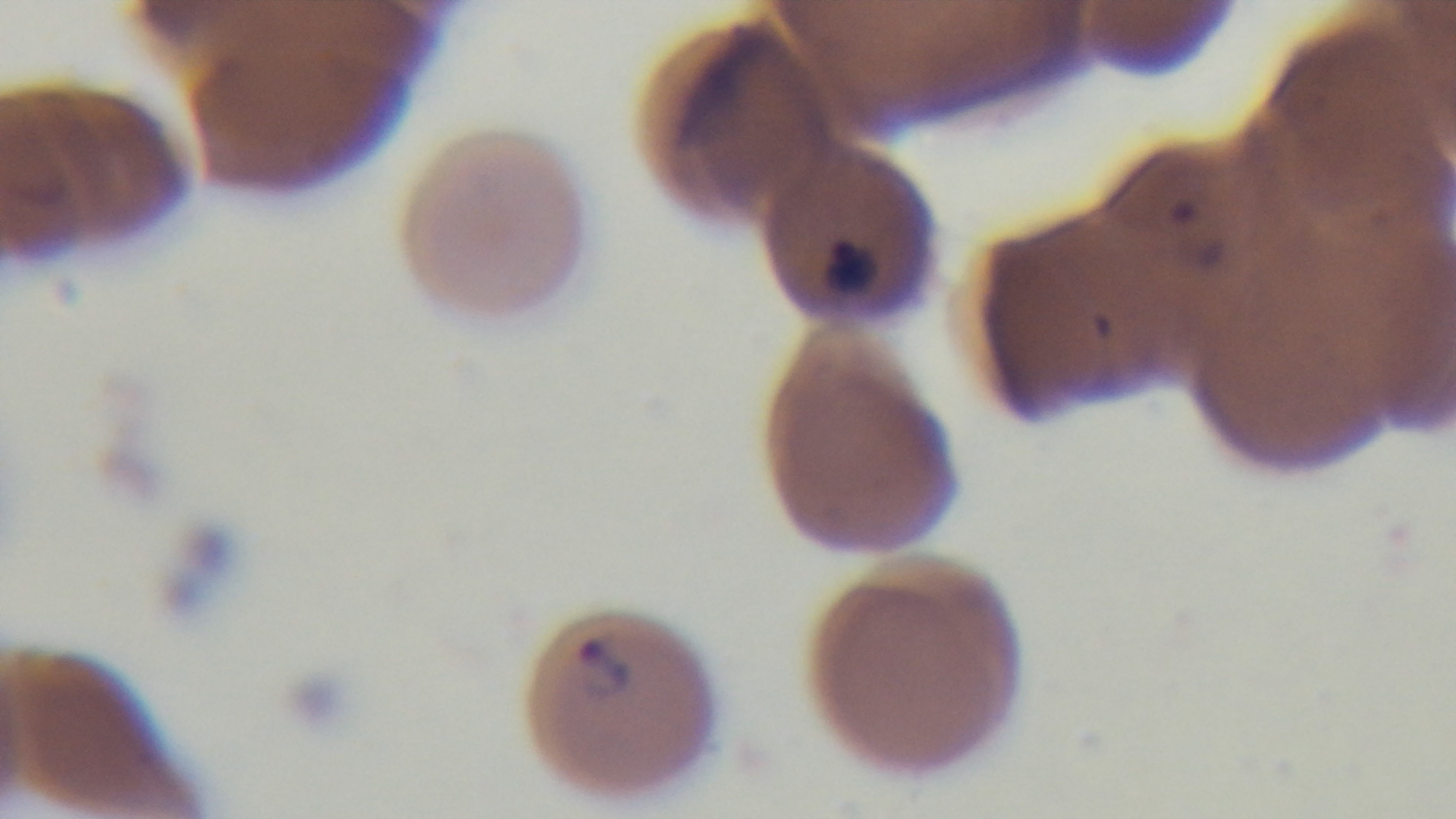
stain = Giemsa
capture = mounted 4K digital camera
malaria status = infected
modality = light microscopy
objective = 100x oil immersion
preparation = thin blood film
field of view = single